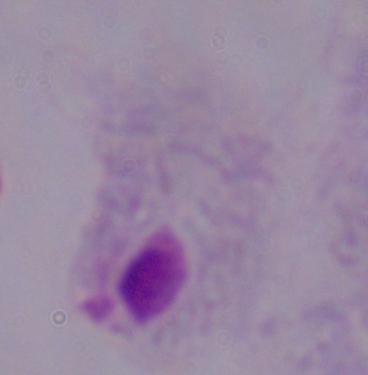
Summary:
  - Modality: micrograph
  - Magnification: 1000x
  - Identification: trichomonad